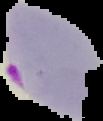

Summary:
  - Image type: segmented cell region with the area outside set to black
  - Preparation: thin blood film
  - Image size: 103×121 pixels
  - Malaria status: parasitized